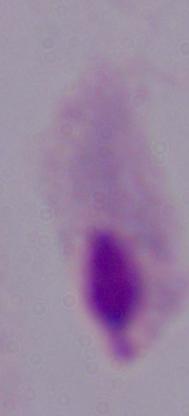 Micrograph. A trichomonad is shown. 1000x magnification.